Locate every malaria parasite.
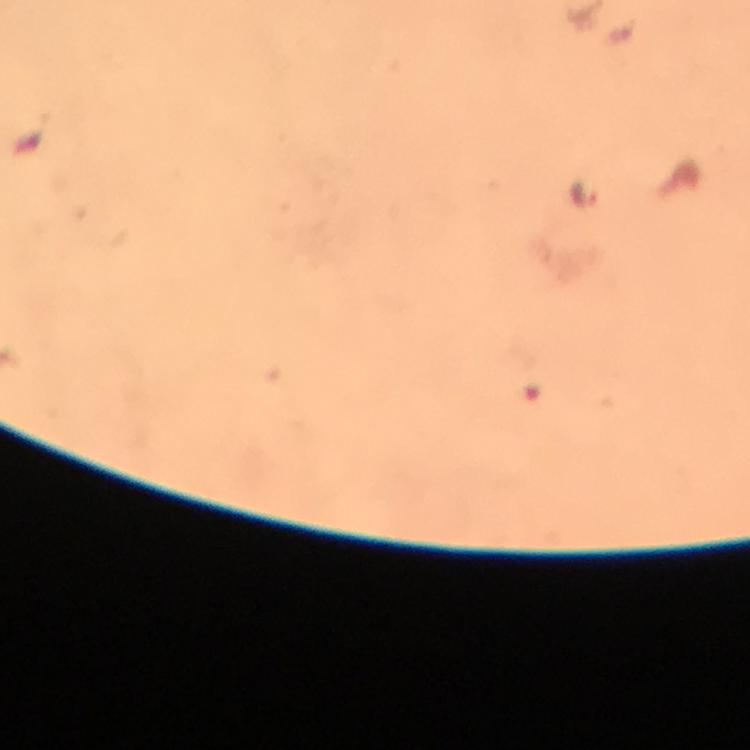
Approximate centers as {x, y} in pixels.
Malaria parasites: {588, 192}.

Summary:
  - Capture: smartphone camera through the microscope
  - Preparation: thick blood film
  - Cropped from: one field of view
  - Context: from a diagnostic examination for malaria
  - Immersion oil: applied
  - Magnification: 100x
  - Image size: 750×750 pixels
  - Stain: Giemsa